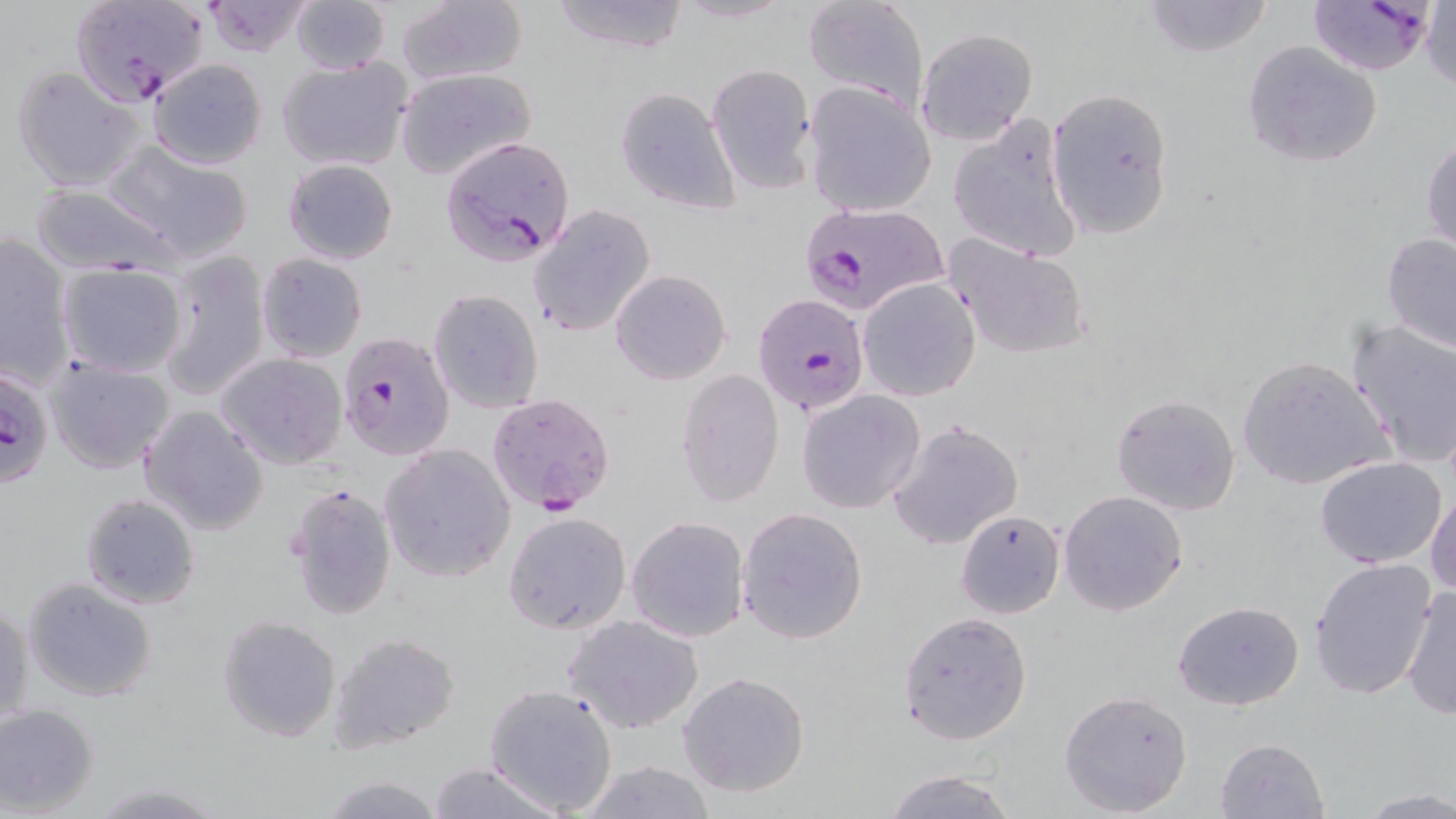
{
  "slide_level_diagnosis": "Plasmodium falciparum",
  "preparation": "thin blood smear",
  "stain": "May-Grünwald-Giemsa",
  "uninfected_red_blood_cell_locations": "approximate bounding boxes as (x1, y1, x2, y2) in pixels: (289, 0, 391, 74), (396, 0, 529, 88), (547, 0, 693, 53), (801, 0, 928, 108), (1140, 0, 1277, 57), (200, 1, 317, 56), (1421, 3, 1456, 92), (916, 27, 1038, 145), (1243, 41, 1383, 167), (276, 55, 414, 172), (148, 58, 268, 170), (9, 64, 147, 193), (705, 64, 816, 193), (395, 68, 536, 179), (802, 81, 938, 216), (1046, 86, 1176, 241), (615, 87, 740, 215), (948, 114, 1084, 263), (1422, 135, 1455, 256), (104, 140, 253, 262), (283, 158, 398, 266), (29, 184, 184, 276), (527, 204, 656, 338), (1381, 231, 1456, 354), (0, 233, 75, 385), (944, 234, 1093, 361), (154, 246, 273, 401), (255, 252, 368, 362), (56, 262, 188, 378), (610, 269, 730, 385), (857, 278, 979, 401), (429, 288, 543, 414), (1345, 318, 1456, 470), (214, 353, 347, 471), (1236, 354, 1392, 491), (43, 355, 175, 474), (676, 366, 785, 509), (797, 389, 925, 513), (1111, 392, 1242, 516), (137, 403, 270, 536), (887, 418, 1025, 550), (378, 442, 516, 582), (1314, 457, 1447, 569), (285, 482, 397, 621), (1059, 489, 1187, 616), (1428, 489, 1456, 599), (79, 493, 201, 610), (736, 507, 869, 645), (955, 509, 1065, 618), (504, 512, 631, 635), (626, 516, 749, 644), (1309, 558, 1438, 701), (23, 577, 159, 703), (1402, 585, 1456, 720), (1, 599, 33, 731), (1174, 601, 1303, 710), (897, 611, 1033, 744), (565, 614, 705, 734), (217, 615, 341, 742), (328, 632, 460, 753), (679, 672, 809, 797), (484, 682, 619, 815), (1058, 689, 1194, 817), (0, 703, 100, 814), (1213, 736, 1331, 819), (576, 760, 720, 818), (425, 762, 563, 819), (882, 769, 1018, 818), (317, 774, 448, 818), (87, 782, 227, 816), (1358, 790, 1456, 817)",
  "modality": "optical microscopy",
  "image_size": "1456×819 pixels",
  "magnification": "1000x",
  "plasmodium_falciparum_infected_red_blood_cell_locations": "approximate bounding boxes as (x1, y1, x2, y2) in pixels: (74, 0, 211, 106), (1308, 1, 1435, 76), (439, 136, 575, 266), (797, 202, 948, 318), (753, 293, 869, 416), (336, 330, 455, 461), (1, 366, 56, 489), (486, 392, 618, 517)",
  "field_of_view": "single"
}